Assess the morphology of the erythrocytes.
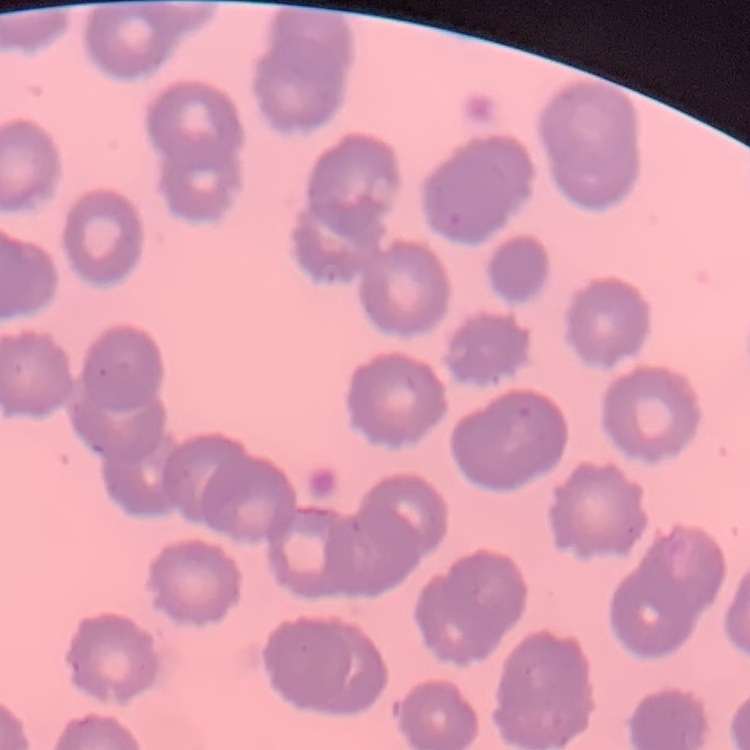
They show no rouleaux formation.

image type = square crop of a larger photomicrograph
stain = Field's or Giemsa
preparation = thin blood film